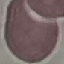
Result: no malaria parasites detected. Acquired by smartphone through the microscope eyepiece. Thin blood smear. Cell patch, automatically extracted from a larger field of view and resized to 64 × 64 pixels. Giemsa stain.